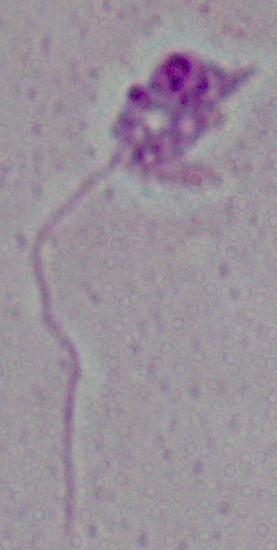 A Leishmania parasite is seen. Micrograph. 1000x magnification.